Locate and identify every blood parasite.
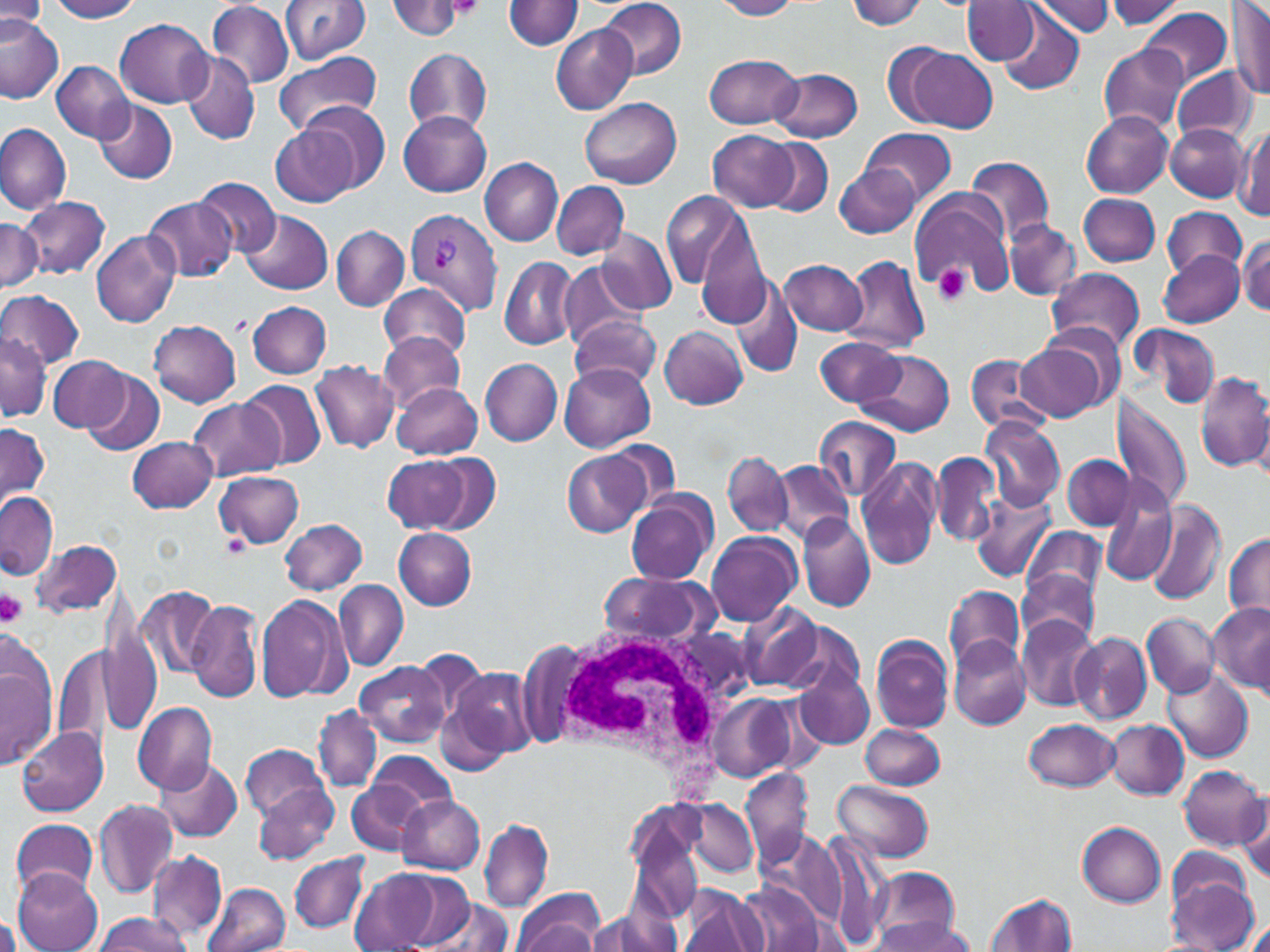

Approximate bounding boxes as (x1, y1, x2, y2) in pixels.
Plasmodium vivax-infected red blood cells: (405, 208, 503, 314).
No Plasmodium falciparum, Plasmodium ovale, Plasmodium malariae, Babesia divergens, or Trypanosoma brucei observed.

Summary:
  - Uninfected red blood cell locations: (279, 0, 370, 64), (597, 0, 688, 80), (711, 0, 803, 20), (1102, 0, 1187, 31), (1228, 0, 1270, 101), (51, 1, 143, 22), (208, 1, 294, 88), (386, 1, 467, 39), (505, 1, 584, 51), (845, 1, 928, 30), (1033, 1, 1115, 38), (1, 3, 45, 36), (963, 3, 1039, 67), (1138, 6, 1231, 89), (995, 7, 1085, 97), (0, 15, 64, 102), (116, 18, 216, 107), (550, 25, 638, 115), (1100, 44, 1188, 133), (900, 47, 996, 133), (403, 48, 492, 135), (272, 51, 381, 138), (180, 52, 259, 146), (704, 54, 803, 130), (51, 60, 132, 143), (1173, 66, 1258, 145), (771, 68, 864, 143), (580, 97, 680, 187), (93, 99, 177, 184), (299, 102, 388, 193), (398, 110, 492, 197), (1081, 112, 1173, 197), (0, 123, 72, 214), (1164, 123, 1251, 202), (1234, 124, 1269, 218), (271, 126, 357, 209), (860, 126, 956, 205), (708, 129, 798, 211), (762, 138, 834, 216), (965, 156, 1056, 244), (478, 157, 563, 246), (835, 164, 920, 240), (193, 177, 280, 258), (552, 181, 629, 260), (909, 189, 1015, 295), (1078, 192, 1161, 267), (661, 193, 750, 292), (20, 195, 110, 280), (144, 196, 237, 282), (1163, 206, 1246, 280), (240, 211, 333, 296), (692, 213, 770, 331), (0, 217, 41, 294), (1003, 218, 1081, 301), (330, 225, 409, 310), (598, 228, 675, 314), (90, 231, 181, 328), (1239, 235, 1268, 316), (1159, 251, 1245, 328), (840, 254, 930, 355), (499, 256, 578, 351), (780, 260, 866, 335), (559, 263, 646, 350), (1046, 268, 1143, 355), (732, 277, 802, 377), (376, 283, 471, 359), (0, 289, 85, 368), (247, 300, 332, 379), (566, 314, 662, 387), (149, 320, 242, 406), (1130, 323, 1221, 408), (659, 325, 748, 410), (377, 330, 466, 413), (0, 333, 50, 421), (815, 337, 906, 408), (1014, 341, 1107, 422), (857, 348, 954, 438), (965, 353, 1052, 435), (49, 355, 131, 432), (480, 357, 562, 447), (309, 361, 400, 452), (559, 363, 655, 453), (82, 368, 165, 455), (1195, 370, 1270, 474), (237, 379, 326, 470), (392, 382, 483, 459), (1113, 394, 1194, 515), (186, 397, 283, 481), (814, 415, 901, 503), (980, 416, 1066, 510), (0, 423, 49, 509), (127, 436, 218, 514), (606, 439, 682, 513), (562, 450, 653, 537), (723, 450, 794, 538), (931, 451, 1000, 547), (428, 455, 500, 533), (1063, 455, 1132, 530), (382, 456, 469, 532), (858, 456, 945, 570), (770, 461, 854, 544), (214, 471, 305, 549), (1101, 482, 1176, 589), (626, 489, 718, 586), (969, 490, 1055, 583), (0, 491, 57, 579), (1145, 499, 1227, 606), (798, 514, 875, 612), (279, 518, 368, 595), (1022, 526, 1105, 604), (393, 528, 477, 610), (705, 530, 802, 626), (1224, 533, 1270, 620), (32, 538, 123, 617), (1018, 569, 1102, 645), (596, 572, 715, 646), (334, 581, 409, 670), (944, 584, 1024, 671), (137, 587, 218, 680), (256, 593, 351, 703), (188, 599, 263, 703), (739, 601, 827, 691), (1208, 601, 1270, 696), (1142, 611, 1218, 698), (99, 615, 161, 737), (1016, 615, 1099, 710), (1070, 631, 1152, 724), (870, 634, 954, 733), (948, 636, 1031, 730), (55, 645, 112, 748), (1, 651, 54, 770), (411, 652, 489, 726), (356, 660, 450, 746), (794, 664, 874, 748), (447, 666, 538, 763), (1164, 669, 1254, 763), (707, 694, 794, 782), (133, 702, 218, 796), (313, 705, 381, 793), (1025, 718, 1120, 792), (1105, 719, 1190, 801), (859, 724, 945, 790), (15, 726, 108, 816), (241, 745, 330, 825), (369, 751, 456, 817), (155, 759, 245, 842), (1179, 765, 1267, 850), (739, 769, 813, 868), (832, 779, 935, 864), (252, 781, 338, 865), (349, 783, 430, 857), (1235, 787, 1270, 883), (397, 795, 485, 873), (675, 796, 760, 880), (95, 798, 179, 897), (626, 811, 706, 922), (480, 818, 554, 912), (10, 819, 100, 899), (1076, 821, 1166, 906), (757, 829, 843, 918), (1166, 845, 1254, 917), (146, 850, 227, 942), (289, 852, 368, 933), (869, 867, 958, 948), (203, 868, 365, 946), (349, 868, 448, 951), (13, 870, 103, 951), (391, 875, 483, 946), (1167, 875, 1260, 952), (736, 880, 827, 952), (202, 883, 291, 952), (678, 887, 767, 952), (514, 889, 603, 952), (985, 893, 1078, 952), (423, 896, 515, 952), (585, 905, 678, 952), (94, 911, 194, 952), (0, 914, 22, 952), (870, 915, 975, 952), (1245, 918, 1270, 951)
  - White blood cell locations: (537, 624, 753, 775)
  - Platelet locations: (442, 0, 486, 20), (934, 266, 970, 306), (0, 588, 28, 628)
  - Slide-level diagnosis: Plasmodium vivax
  - Image size: 1270×952 pixels
  - Stain: May-Grünwald-Giemsa
  - Modality: optical microscopy
  - Field of view: one of a larger specimen
  - Magnification: 1000x
  - Preparation: thin blood film